Give the extent of all Plasmodium vivax-infected red blood cells.
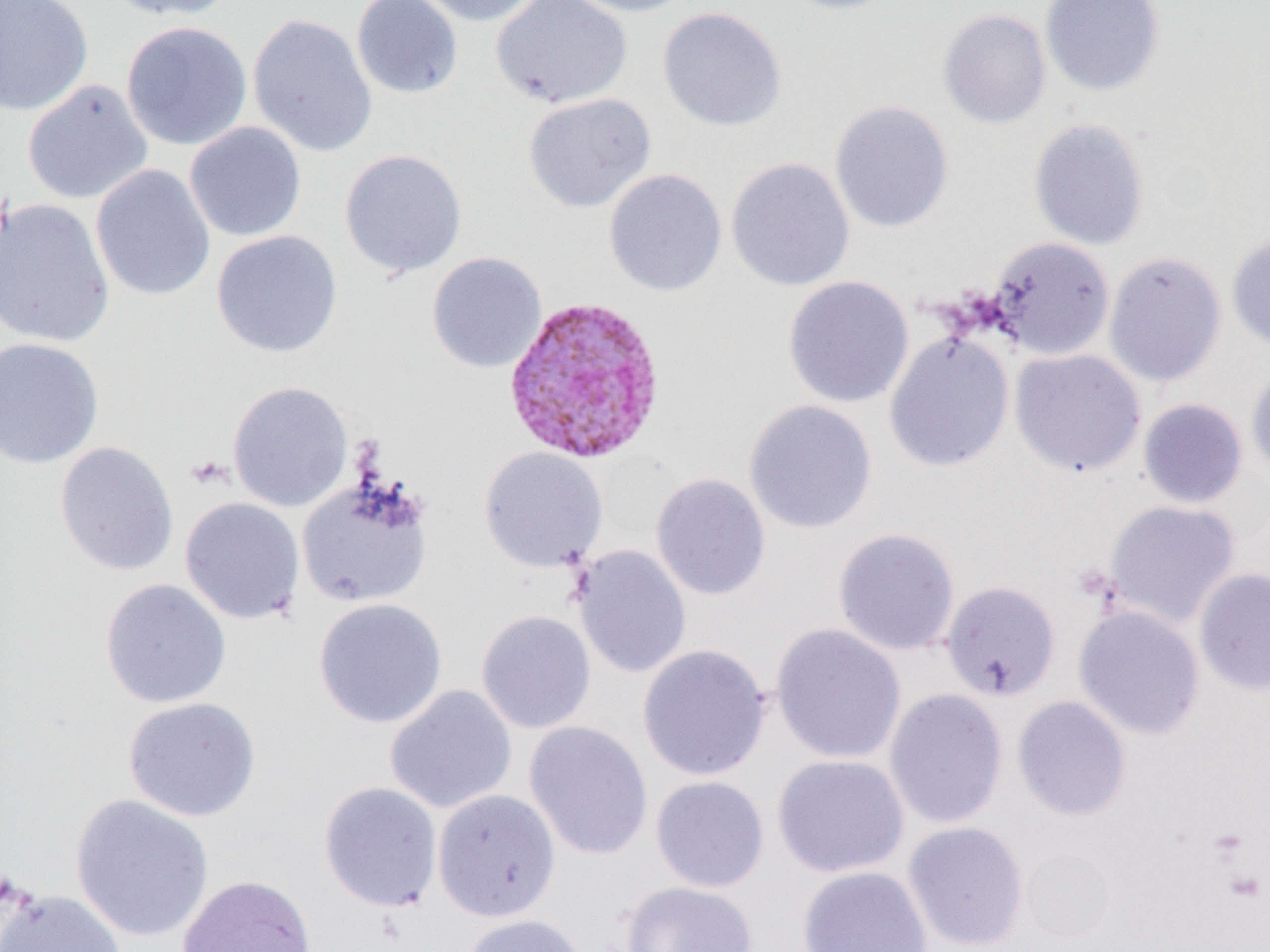
Approximate bounding boxes as [x1, y1, x2, y2] in pixels.
Plasmodium vivax-infected red blood cells: [502, 295, 668, 464].

slide-level diagnosis = Plasmodium vivax
uninfected red blood cell locations = approximate bounding boxes as [x1, y1, x2, y2] in pixels: [0, 0, 94, 117], [100, 0, 236, 20], [351, 0, 464, 100], [407, 0, 542, 27], [491, 0, 633, 110], [559, 0, 697, 17], [774, 0, 907, 15], [1039, 0, 1164, 97], [657, 6, 787, 132], [937, 8, 1051, 130], [248, 13, 378, 158], [121, 21, 252, 151], [22, 79, 154, 205], [523, 92, 656, 213], [829, 100, 954, 234], [1028, 118, 1150, 251], [184, 121, 306, 242], [339, 148, 468, 279], [725, 157, 855, 292], [90, 164, 216, 302], [604, 168, 727, 297], [0, 198, 115, 348], [210, 230, 343, 358], [1225, 233, 1270, 351], [986, 236, 1115, 360], [1104, 251, 1226, 387], [426, 252, 547, 373], [782, 275, 914, 409], [884, 331, 1014, 472], [0, 337, 104, 470], [1010, 348, 1146, 477], [1246, 361, 1270, 479], [227, 380, 353, 512], [1137, 398, 1248, 508], [744, 399, 878, 534], [54, 441, 179, 577], [478, 447, 609, 573], [650, 472, 771, 600], [296, 478, 433, 608], [179, 496, 305, 624], [1103, 500, 1241, 629], [833, 527, 960, 656], [572, 545, 692, 679], [1194, 568, 1270, 695], [99, 578, 232, 709], [940, 580, 1061, 701], [313, 597, 448, 729], [1074, 604, 1205, 740], [476, 609, 596, 734], [770, 623, 906, 764], [637, 644, 771, 781], [384, 684, 517, 814], [884, 688, 1007, 829], [1011, 695, 1131, 821], [123, 696, 261, 822], [524, 720, 653, 860], [772, 753, 910, 878], [650, 775, 770, 892], [319, 781, 443, 912], [432, 788, 561, 922], [70, 794, 214, 942], [902, 820, 1029, 951], [1018, 847, 1121, 946], [797, 865, 933, 952], [177, 874, 316, 952], [619, 880, 759, 952], [1, 889, 126, 952], [459, 913, 589, 952]
platelet locations = approximate bounding boxes as [x1, y1, x2, y2] in pixels: [186, 455, 231, 491]
image size = 1270×952 pixels
preparation = thin blood smear
field of view = one of a larger specimen
magnification = 1000x
modality = optical microscopy